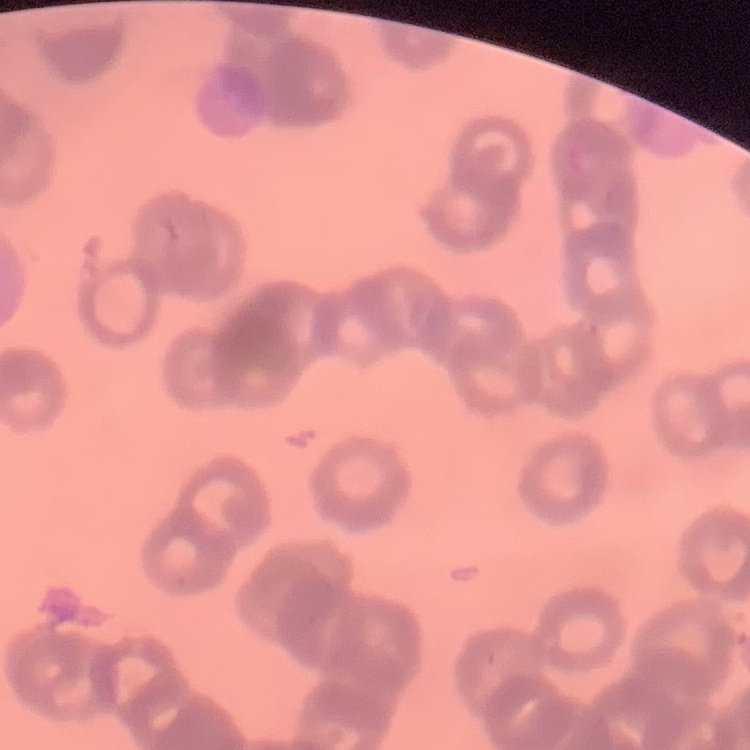

The erythrocytes exhibit rouleaux formation. Field's or Giemsa stain. Square crop of a larger photomicrograph. Thin blood film.